Give the extent of all uninfected red blood cells.
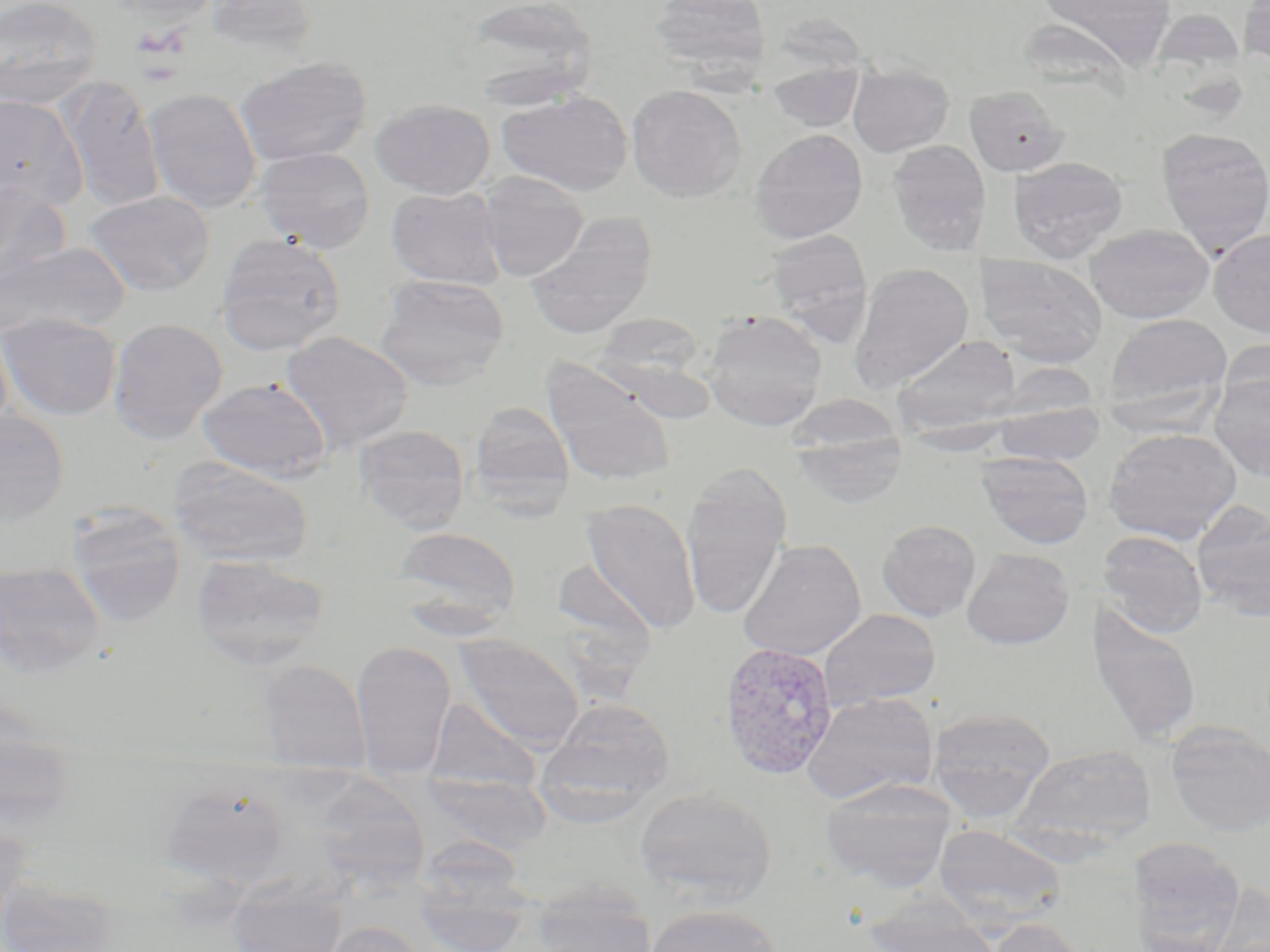

Approximate bounding boxes as (x1, y1, x2, y2) in pixels.
Uninfected red blood cells: (0, 0, 101, 108), (113, 0, 223, 27), (459, 0, 598, 109), (651, 0, 772, 77), (1030, 0, 1180, 71), (204, 1, 319, 55), (235, 56, 372, 166), (766, 63, 866, 132), (847, 65, 954, 157), (61, 77, 166, 212), (626, 84, 746, 202), (964, 86, 1068, 176), (144, 87, 263, 213), (498, 91, 633, 196), (0, 94, 85, 209), (372, 99, 495, 199), (1156, 127, 1270, 256), (750, 129, 868, 243), (887, 140, 991, 256), (255, 146, 375, 253), (1008, 156, 1128, 263), (479, 171, 589, 281), (0, 181, 70, 290), (386, 186, 506, 289), (85, 190, 215, 296), (525, 216, 656, 339), (1086, 223, 1213, 323), (764, 228, 874, 344), (1209, 228, 1270, 337), (215, 232, 346, 355), (1, 242, 131, 339), (975, 254, 1108, 366), (850, 261, 974, 391), (376, 275, 509, 389), (702, 310, 828, 430), (0, 312, 121, 420), (1103, 312, 1233, 416), (593, 313, 707, 386), (108, 317, 228, 443), (280, 331, 414, 452), (892, 335, 1023, 434), (1218, 339, 1270, 419), (545, 366, 676, 488), (1210, 374, 1270, 480), (197, 377, 332, 481), (469, 401, 575, 512), (994, 401, 1104, 466), (0, 411, 69, 524), (355, 424, 470, 533), (790, 424, 907, 509), (1103, 427, 1242, 545), (976, 451, 1094, 549), (169, 457, 314, 567), (680, 465, 791, 621), (580, 498, 702, 635), (1192, 502, 1270, 621), (67, 504, 186, 626), (877, 520, 981, 622), (392, 526, 521, 625), (1097, 531, 1208, 637), (737, 538, 867, 661), (961, 549, 1075, 650), (192, 553, 329, 669), (553, 559, 658, 655), (0, 562, 104, 676), (1086, 603, 1203, 746), (818, 609, 941, 713), (453, 634, 585, 749), (351, 641, 456, 779), (258, 659, 371, 774), (802, 692, 939, 804), (427, 697, 541, 794), (539, 697, 675, 821), (928, 706, 1056, 823), (0, 717, 79, 835), (1166, 725, 1270, 837), (1013, 743, 1157, 848), (422, 772, 551, 855), (819, 777, 958, 892), (160, 783, 288, 886), (634, 786, 776, 907), (0, 821, 30, 935), (933, 824, 1066, 931), (415, 835, 530, 913), (1126, 838, 1246, 952), (0, 878, 117, 952), (226, 879, 349, 952), (1209, 883, 1270, 952), (410, 884, 533, 952), (529, 885, 658, 952), (863, 896, 1002, 952), (643, 903, 782, 952), (987, 918, 1091, 952), (320, 919, 432, 952).

Summary:
  - Plasmodium vivax-infected red blood cell locations: (721, 644, 844, 782)
  - Slide-level diagnosis: Plasmodium vivax
  - Field of view: one of a larger specimen
  - Preparation: thin blood film
  - Image size: 1270×952 pixels
  - Modality: light microscopy
  - Magnification: 1000x
  - Stain: May-Grünwald-Giemsa